Assess the morphology of the red blood cells.
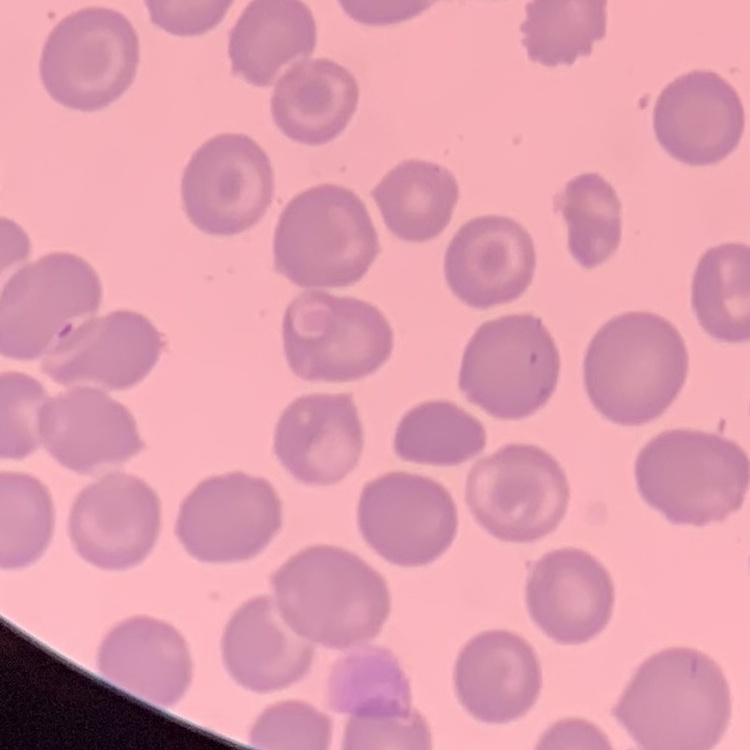

No rouleaux formation.

Summary:
  - Image type: square crop of a larger photomicrograph
  - Preparation: thin blood film
  - Stain: Field's or Giemsa